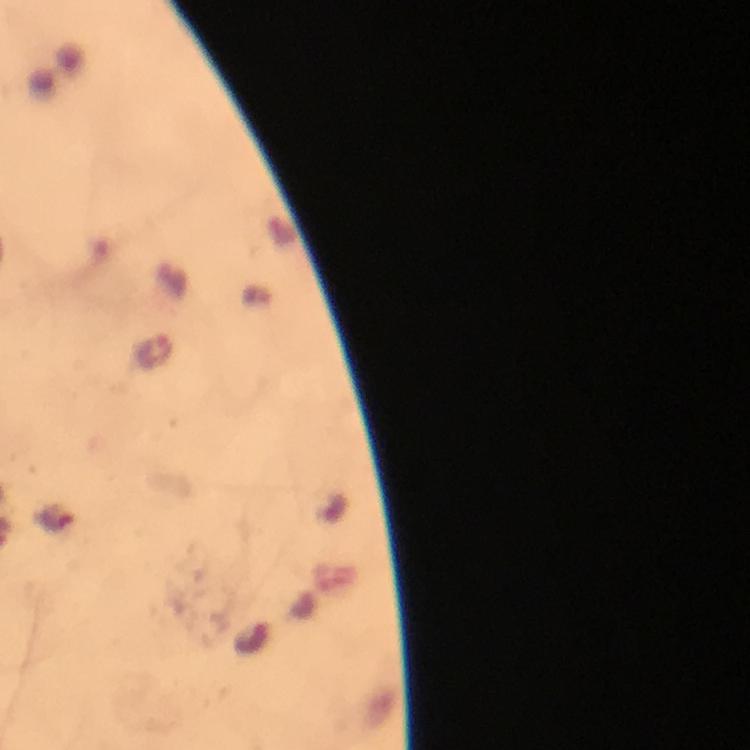
{
  "plasmodium_parasite_locations": "approximate centers as [x, y] in pixels: [153, 349]",
  "capture": "smartphone photograph through a microscope",
  "image_size": "750×750 pixels",
  "cropped_from": "a single field of view",
  "magnification": "100x",
  "stain": "Giemsa",
  "preparation": "thick blood film",
  "context": "from a diagnostic examination for malaria",
  "immersion_oil": "used"
}